Identify the preparation type.
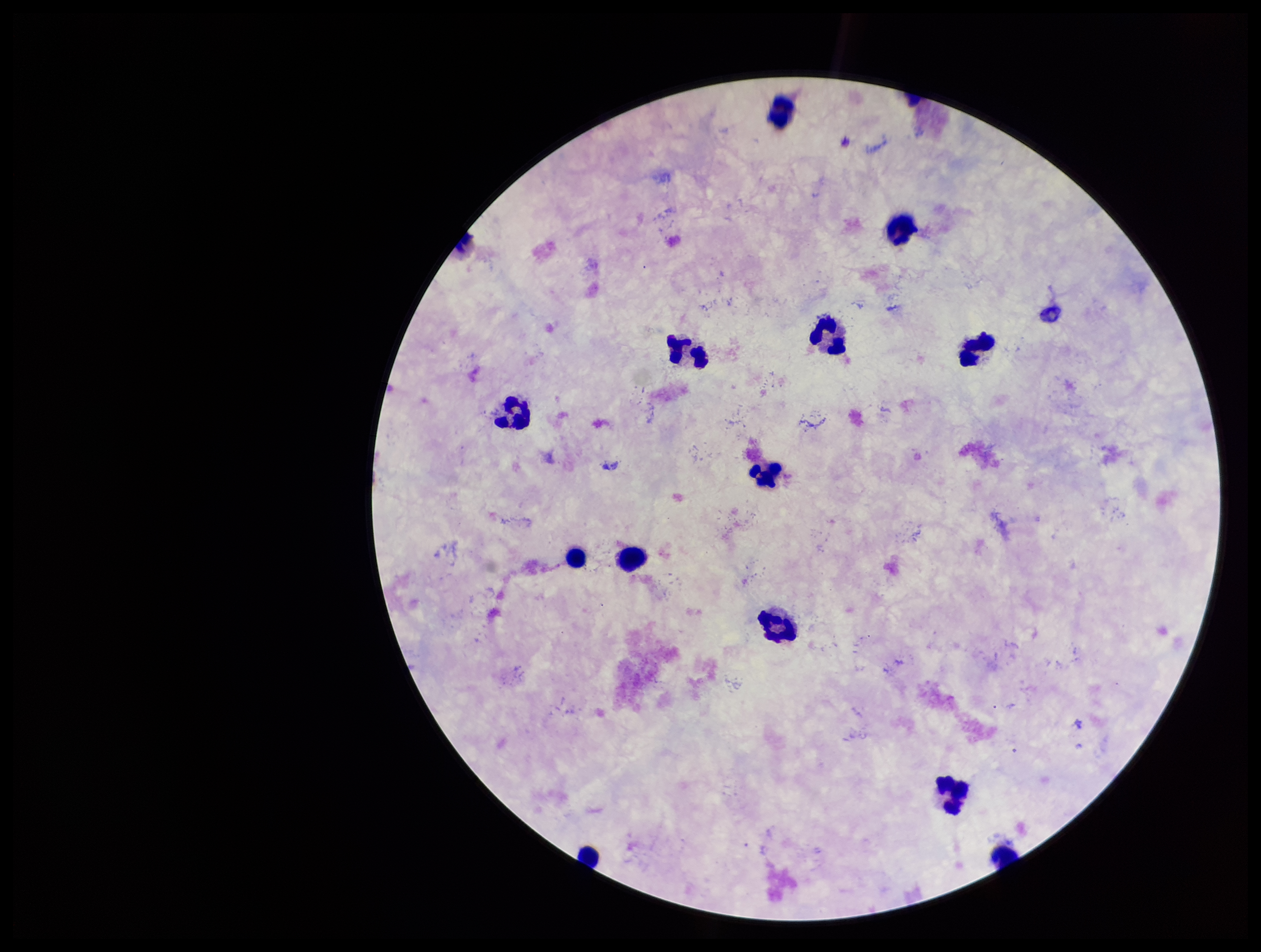

Thick.

Leukocyte count: 12. Giemsa stain. Single field of view. Photographed through the microscope eyepiece with a smartphone camera. Plasmodium parasites: none detected. Parasite count: 0. Patient malaria status: negative. Image is 1261×952 pixels.